Report the malaria status.
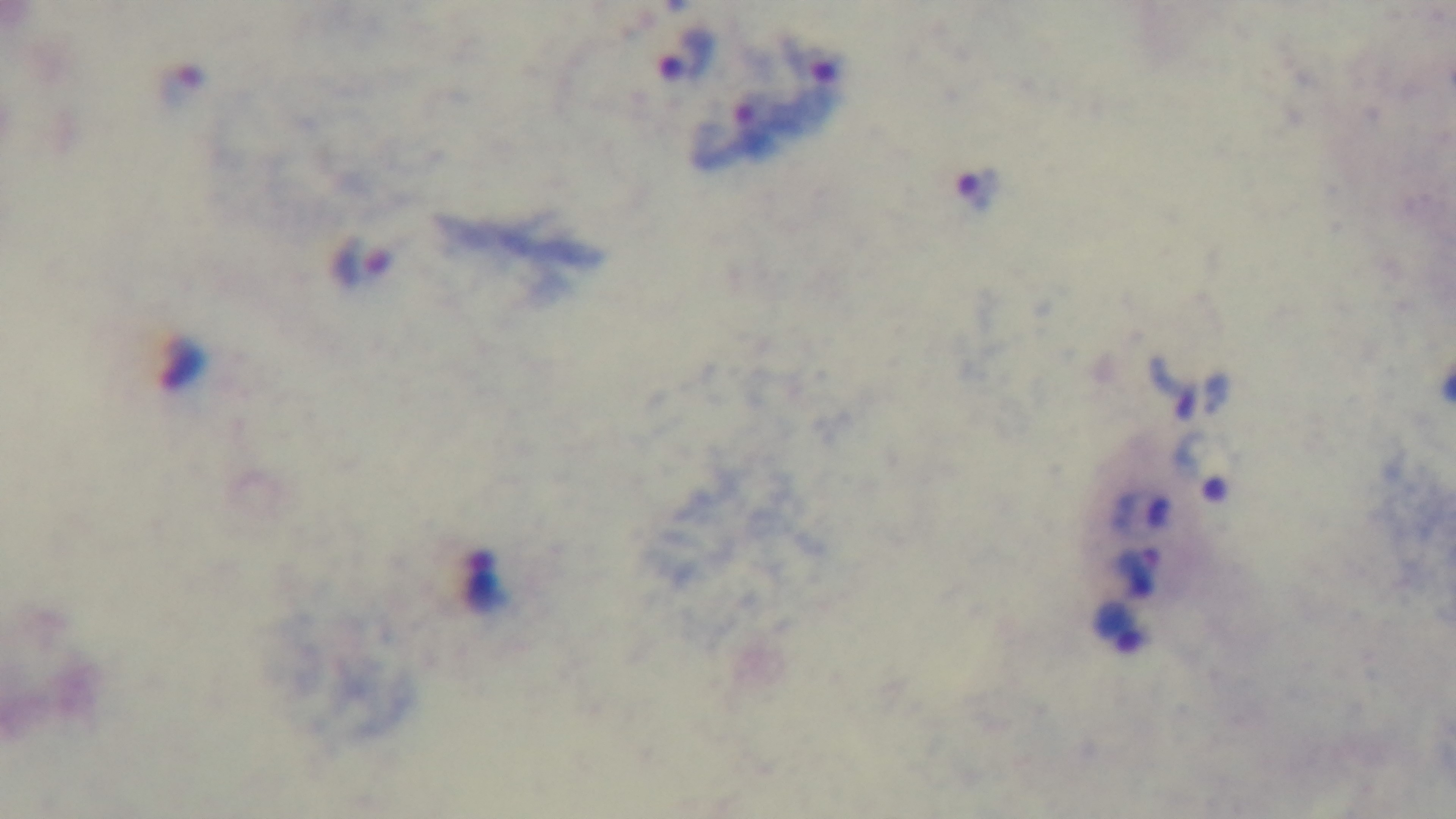

It is infected.

Summary:
  - Modality: light microscopy
  - Preparation: thick blood film
  - Capture: mounted 4K digital camera
  - Field of view: one from the slide
  - Stain: Giemsa
  - Objective: 100x oil immersion